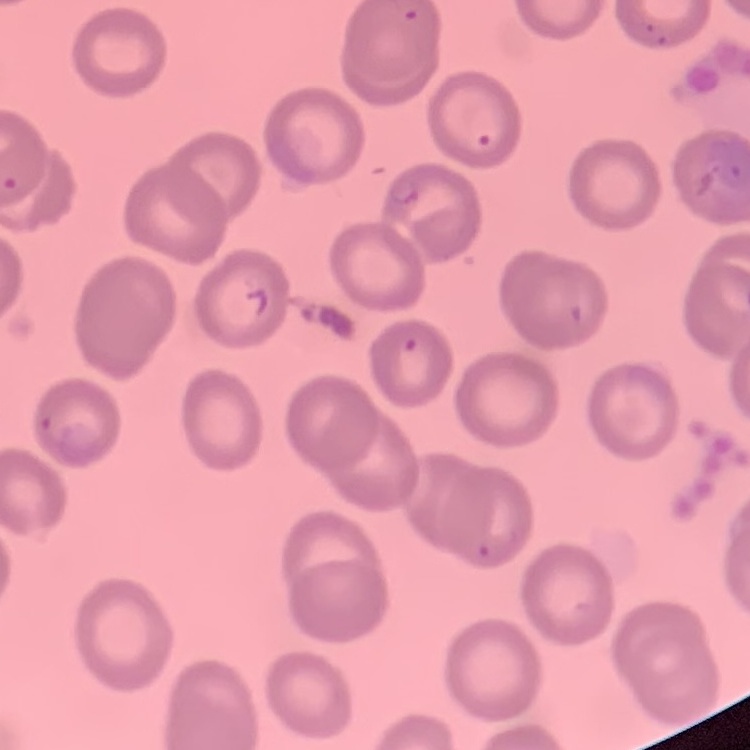
The red blood cells show no rouleaux formation. Thin blood smear. Square crop of a larger photomicrograph. Field's or Giemsa stain.